State which parasite is depicted.
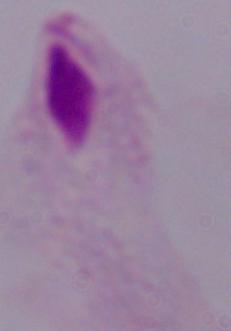
This is a trichomonad.

magnification = 1000x
modality = photomicrograph